Assess this cell for malaria.
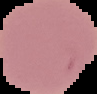

It is uninfected.

Image is 97×94 pixels. Segmented cell region on a black background. From a thin blood smear.